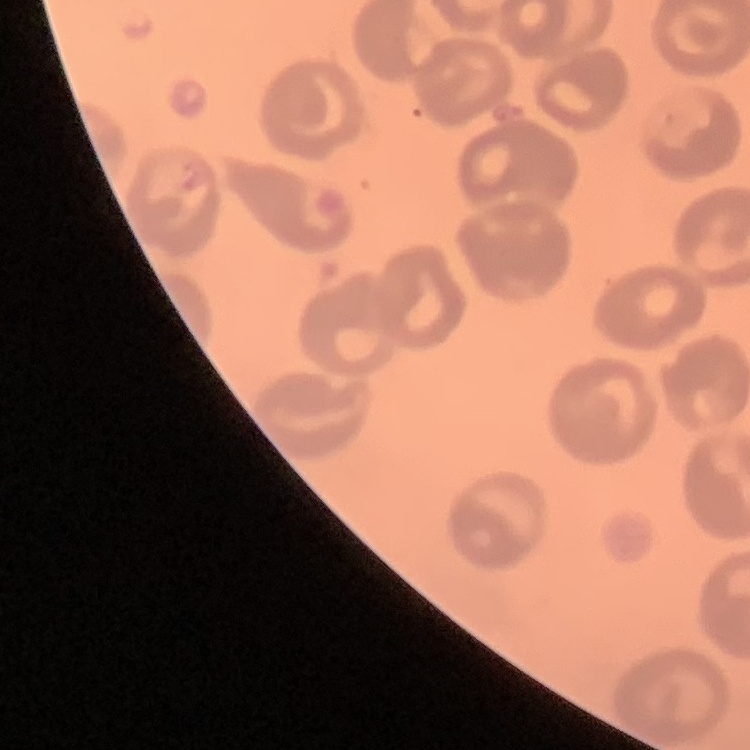 The erythrocytes exhibit no rouleaux formation. Stained with either Field's or Giemsa. Thin blood smear. Square crop of a larger photomicrograph.